State the blood parasite species.
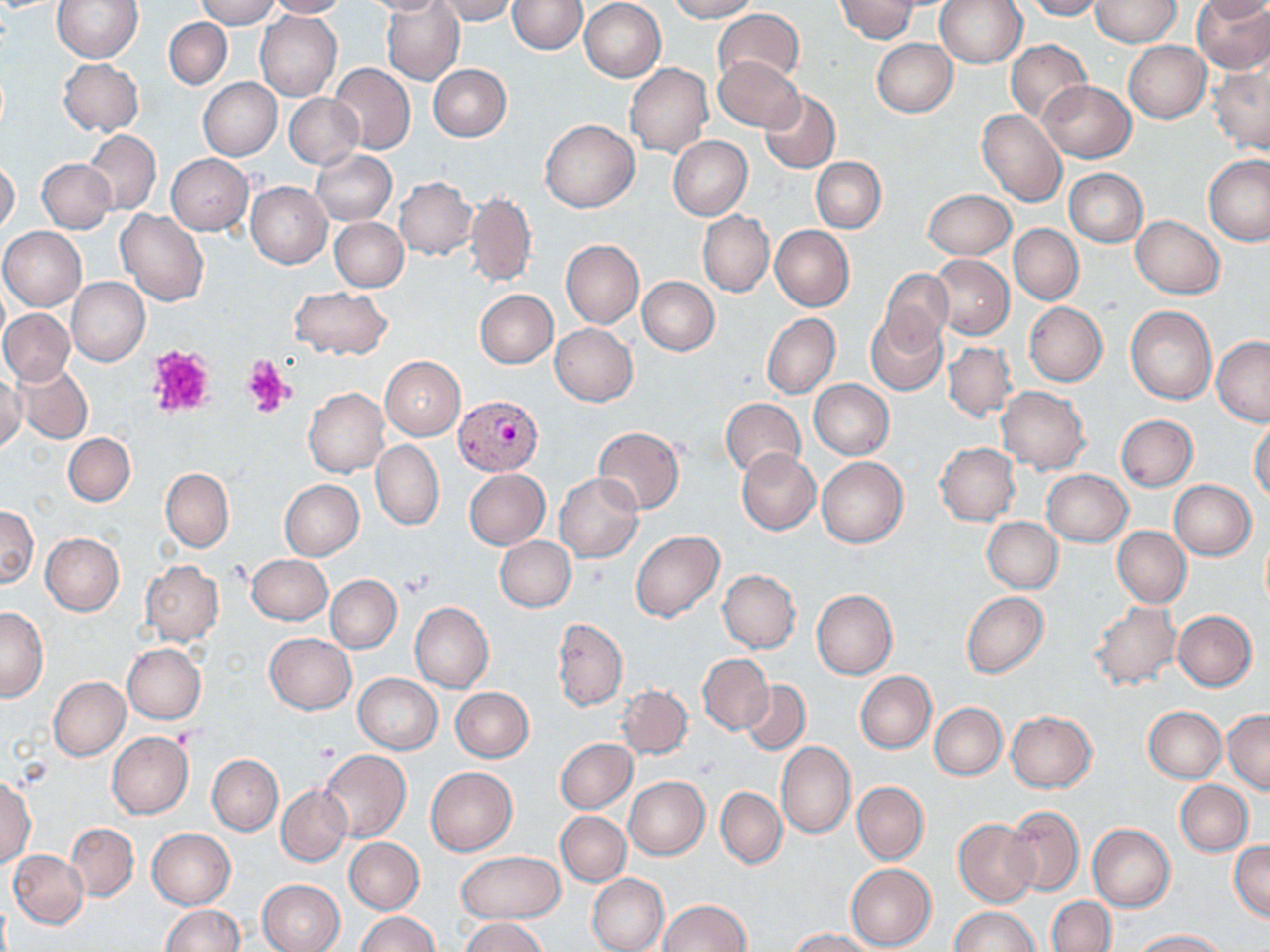

Plasmodium vivax.

uninfected red blood cell locations = approximate bounding boxes as (x1, y1, x2, y2) in pixels: (52, 0, 142, 63), (195, 0, 279, 28), (264, 0, 348, 18), (359, 0, 449, 16), (381, 0, 465, 85), (432, 0, 518, 24), (509, 0, 586, 53), (665, 0, 758, 22), (835, 0, 918, 42), (934, 0, 1026, 69), (1024, 0, 1101, 20), (1192, 0, 1270, 73), (1197, 0, 1269, 23), (579, 1, 665, 81), (1090, 1, 1181, 47), (714, 8, 802, 86), (255, 11, 341, 101), (163, 17, 232, 90), (870, 38, 957, 117), (1005, 39, 1091, 125), (1123, 41, 1210, 122), (713, 56, 804, 132), (58, 57, 144, 135), (329, 63, 415, 155), (428, 63, 512, 141), (624, 63, 712, 158), (1210, 63, 1270, 155), (199, 78, 282, 160), (1039, 81, 1134, 161), (759, 90, 840, 172), (284, 93, 363, 169), (977, 109, 1067, 208), (540, 119, 639, 212), (84, 130, 161, 214), (668, 136, 753, 219), (312, 150, 396, 225), (166, 154, 253, 234), (1204, 155, 1270, 245), (37, 157, 115, 233), (812, 157, 885, 233), (0, 160, 20, 235), (1064, 168, 1147, 247), (393, 177, 477, 260), (245, 182, 331, 268), (465, 188, 537, 288), (923, 188, 1016, 259), (117, 210, 208, 306), (698, 211, 774, 296), (1131, 216, 1224, 299), (330, 217, 408, 291), (770, 225, 854, 311), (1009, 225, 1083, 305), (1, 226, 86, 312), (560, 240, 643, 328), (930, 255, 1013, 339), (879, 268, 954, 350), (638, 276, 719, 355), (66, 277, 149, 366), (289, 286, 394, 359), (475, 289, 558, 368), (1, 297, 143, 378), (1024, 302, 1107, 386), (1125, 305, 1217, 404), (0, 309, 74, 385), (762, 312, 840, 398), (865, 313, 946, 395), (550, 323, 637, 406), (1211, 336, 1270, 425), (943, 340, 1017, 422), (380, 356, 465, 440), (12, 361, 92, 443), (0, 375, 26, 454), (809, 379, 894, 458), (996, 386, 1091, 473), (304, 388, 389, 477), (721, 398, 806, 479), (1115, 415, 1197, 492), (1249, 416, 1270, 502), (593, 427, 684, 514), (63, 433, 135, 506), (371, 439, 444, 529), (936, 441, 1021, 525), (736, 448, 821, 535), (816, 457, 908, 547), (161, 467, 233, 553), (464, 469, 550, 550), (1042, 469, 1132, 546), (555, 472, 643, 563), (280, 480, 364, 560), (1169, 480, 1256, 559), (1, 506, 38, 587), (982, 516, 1062, 593), (1113, 527, 1190, 607), (630, 529, 724, 622), (41, 533, 124, 615), (1260, 535, 1270, 612), (495, 537, 575, 612), (246, 554, 331, 625), (139, 560, 225, 646), (718, 569, 800, 653), (325, 575, 401, 653), (811, 589, 897, 679), (961, 592, 1049, 678), (1089, 601, 1180, 690), (409, 602, 493, 693), (0, 607, 50, 701), (1172, 610, 1256, 691), (553, 618, 627, 711), (264, 633, 356, 713), (122, 643, 205, 724), (697, 654, 773, 733), (854, 671, 936, 753), (354, 673, 442, 754), (49, 676, 130, 761), (741, 680, 810, 754), (616, 685, 692, 759), (452, 687, 533, 762), (930, 703, 1006, 780), (1144, 706, 1226, 782), (1223, 710, 1270, 792), (1006, 711, 1097, 792), (106, 731, 194, 819), (556, 738, 637, 813), (776, 742, 855, 839), (319, 749, 410, 841), (207, 754, 283, 835), (426, 767, 517, 855), (0, 776, 35, 870), (624, 776, 710, 859), (1175, 780, 1253, 856), (852, 781, 928, 864), (276, 785, 352, 867), (716, 787, 787, 869), (1003, 805, 1083, 896), (555, 811, 631, 885), (955, 818, 1039, 907), (66, 823, 138, 901), (1088, 824, 1175, 911), (148, 828, 236, 910), (344, 837, 424, 914), (1230, 842, 1269, 921), (9, 850, 88, 927), (457, 851, 564, 924), (846, 863, 936, 951), (587, 873, 669, 952), (258, 878, 345, 952), (1047, 897, 1116, 952), (658, 899, 750, 951), (160, 904, 243, 952), (949, 907, 1039, 952), (356, 912, 439, 952), (459, 916, 548, 952), (790, 928, 876, 952), (1133, 929, 1229, 952)
image size = 1270×952 pixels
modality = light microscopy
Plasmodium vivax-infected red blood cell locations = approximate bounding boxes as (x1, y1, x2, y2) in pixels: (456, 396, 544, 475)
field of view = one of a larger specimen
platelet locations = approximate bounding boxes as (x1, y1, x2, y2) in pixels: (146, 343, 218, 418), (242, 357, 291, 418), (315, 739, 341, 761)
preparation = thin blood smear
magnification = 1000x
stain = May-Grünwald-Giemsa